Identify the cell.
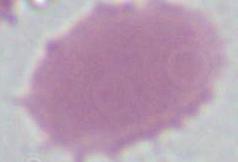
An erythrocyte.

Summary:
  - Modality: photomicrograph
  - Magnification: 1000x